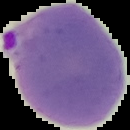 From a thin blood smear. Result: Plasmodium parasites detected. Cell region segmented out of the field of view; the surrounding area is masked to black. Image is 130×130 pixels.